Assess for Plasmodium parasites.
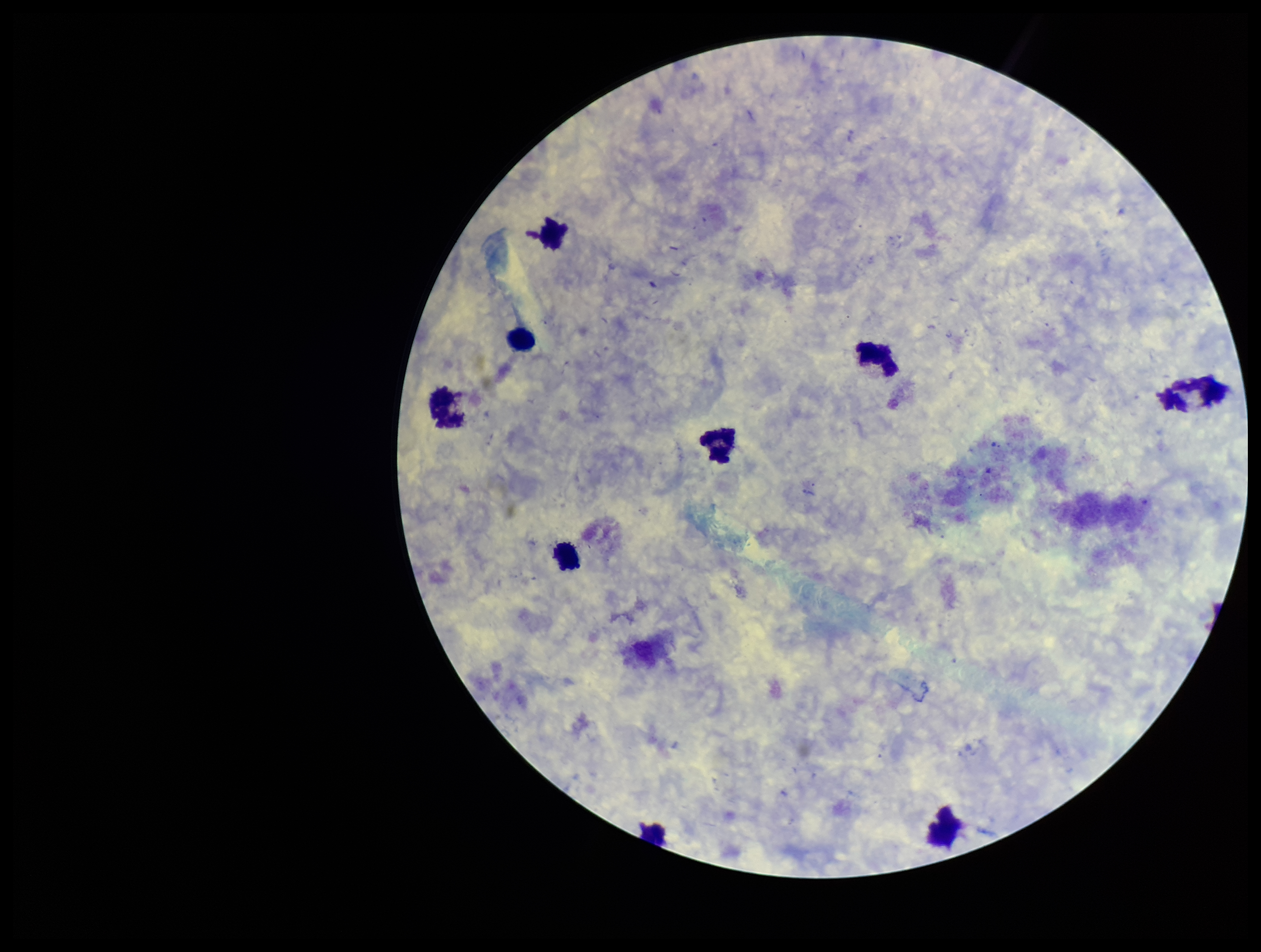
None seen.

Single field of view. Giemsa stain. Smartphone photograph taken through the eyepiece of a microscope. Leukocyte count: 9. Image is 1261×952 pixels. Patient malaria status: negative. Preparation: thick. Parasite count: 0.